Name the parasite shown.
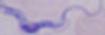

This is a trypanosome.

Photomicrograph. 1000x magnification.